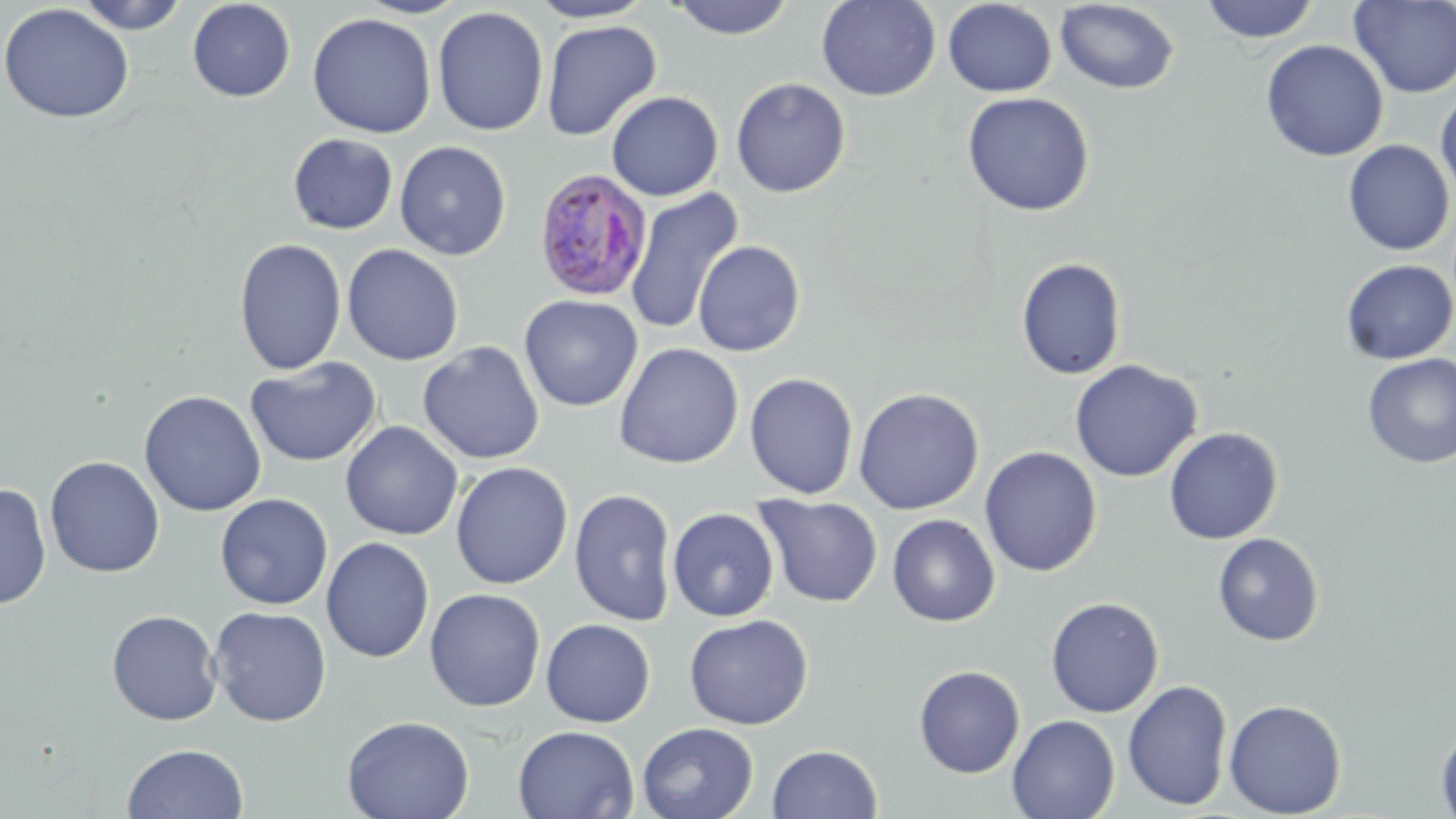

{
  "slide_level_diagnosis": "Plasmodium ovale",
  "image_size": "1456×819 pixels",
  "magnification": "1000x",
  "uninfected_red_blood_cell_locations": "approximate bounding boxes as (x1,y1)-(x2,y2) corner pairs in pixels: (73,0)-(191,34), (187,0)-(296,102), (354,0)-(471,19), (527,0)-(654,23), (667,0)-(797,40), (816,0)-(941,102), (1349,0)-(1456,97), (942,1)-(1057,97), (1054,1)-(1180,94), (1200,1)-(1320,44), (0,3)-(135,124), (432,6)-(548,137), (307,12)-(436,138), (541,19)-(661,142), (1260,39)-(1388,162), (731,77)-(850,198), (606,91)-(723,201), (1435,91)-(1456,201), (962,92)-(1094,217), (287,133)-(398,235), (1343,140)-(1454,255), (394,141)-(511,261), (625,187)-(744,336), (233,238)-(346,376), (692,240)-(805,357), (341,244)-(464,366), (1016,258)-(1126,379), (1340,260)-(1456,365), (519,294)-(642,412), (418,341)-(544,465), (614,343)-(743,469), (1362,354)-(1456,468), (245,357)-(381,468), (1069,359)-(1202,482), (744,373)-(858,500), (853,388)-(984,515), (138,390)-(266,517), (340,421)-(463,541), (1163,427)-(1282,544), (979,446)-(1102,577), (44,456)-(165,578), (450,462)-(573,589), (0,482)-(52,611), (569,488)-(677,627), (215,493)-(333,610), (754,494)-(883,608), (667,508)-(779,622), (887,514)-(1000,627), (1212,533)-(1323,646), (320,537)-(434,663), (425,588)-(546,711), (1045,597)-(1164,717), (209,606)-(332,726), (107,609)-(223,725), (684,614)-(813,730), (541,618)-(655,727), (913,664)-(1025,778), (1122,679)-(1232,811), (1223,699)-(1347,817), (1007,714)-(1120,819), (342,715)-(474,819), (637,722)-(759,819), (1435,722)-(1456,819), (513,725)-(639,819), (122,743)-(249,819), (767,744)-(882,819)",
  "stain": "May-Grünwald-Giemsa",
  "field_of_view": "one of a larger specimen",
  "plasmodium_ovale_infected_red_blood_cell_locations": "approximate bounding boxes as (x1,y1)-(x2,y2) corner pairs in pixels: (532,168)-(653,302)",
  "modality": "light microscopy",
  "preparation": "thin blood smear"
}